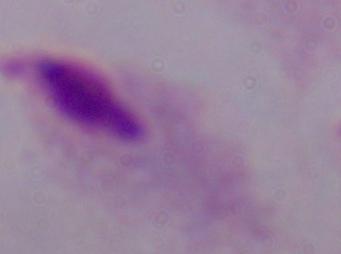

Captured at 1000x magnification. Photomicrograph. A trichomonad is shown.